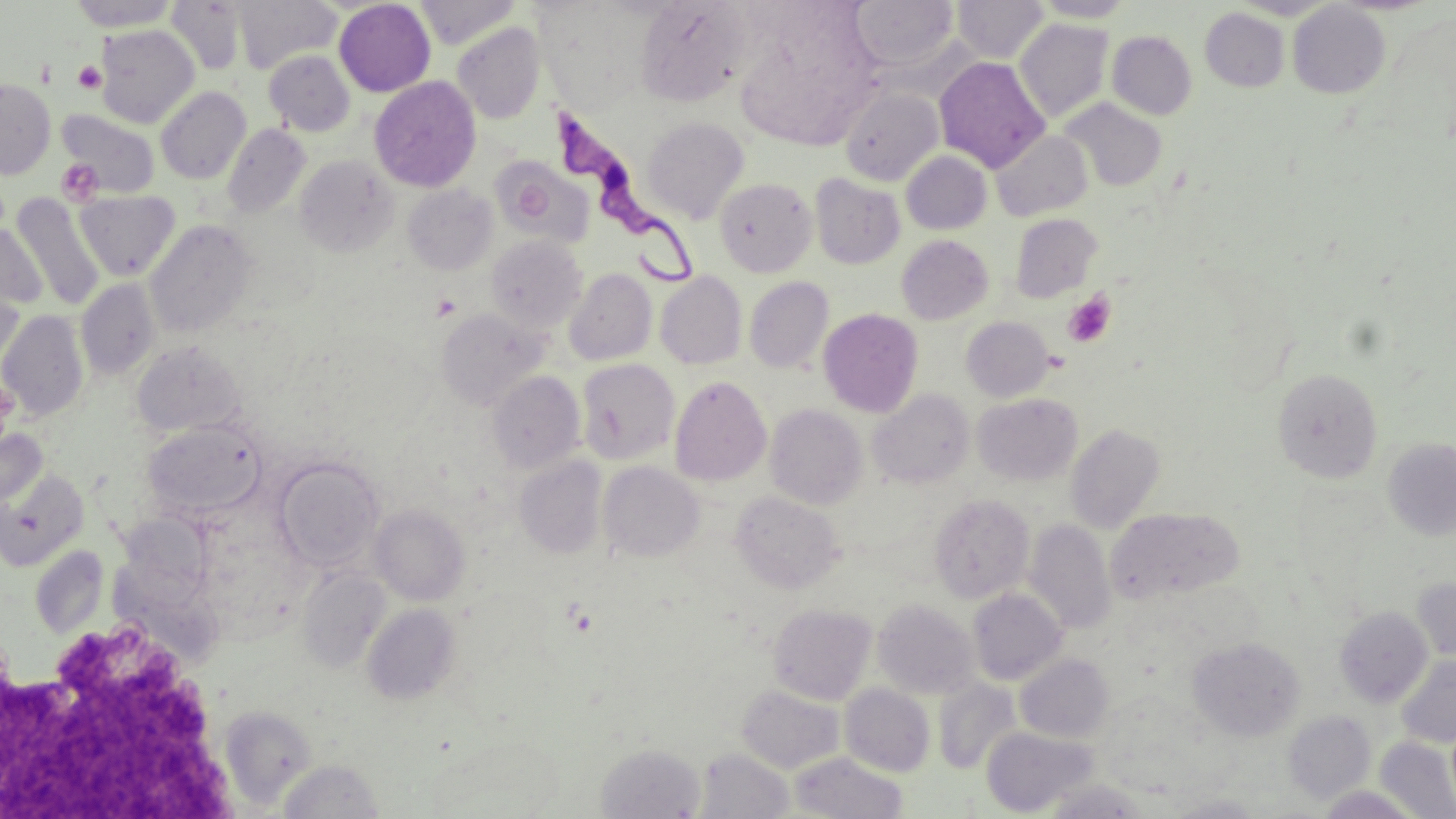
slide_level_diagnosis: Trypanosoma brucei
magnification: 1000x
preparation: thin blood smear
trypanosoma_brucei_locations: 'approximate bounding boxes as (x1,y1)-(x2,y2) corner pairs in pixels: (552,105)-(702,290)'
image_size: 1456×819 pixels
uninfected_red_blood_cell_locations: 'approximate bounding boxes as (x1,y1)-(x2,y2) corner pairs in pixels: (68,0)-(178,31), (233,0)-(341,74), (414,0)-(519,49), (635,0)-(750,106), (952,0)-(1049,63), (166,1)-(246,75), (334,1)-(436,97), (851,1)-(958,71), (1031,1)-(1137,22), (1288,2)-(1390,98), (1200,8)-(1290,92), (1013,18)-(1114,123), (451,22)-(545,124), (95,25)-(199,128), (1107,31)-(1197,119), (263,50)-(355,136), (935,56)-(1050,172), (369,76)-(481,192), (0,79)-(56,179), (156,86)-(251,184), (840,87)-(943,186), (1061,98)-(1167,191), (58,109)-(160,199), (642,116)-(749,223), (222,124)-(311,218), (991,130)-(1093,221), (902,151)-(991,234), (294,154)-(399,257), (491,157)-(594,247), (810,173)-(905,269), (715,177)-(817,277), (402,184)-(497,275), (74,191)-(180,281), (8,194)-(106,310), (1009,213)-(1103,302), (145,219)-(257,338), (0,224)-(47,314), (485,235)-(587,333), (896,235)-(993,325), (1,268)-(27,371), (564,268)-(656,366), (655,272)-(748,369), (744,276)-(834,373), (75,279)-(160,380), (436,308)-(549,410), (818,308)-(923,417), (0,311)-(88,421), (961,316)-(1054,402), (132,341)-(246,437), (576,359)-(680,465), (1273,368)-(1383,482), (486,370)-(585,474), (670,376)-(772,487), (868,389)-(974,489), (972,393)-(1082,486), (765,403)-(868,510), (143,419)-(266,519), (1066,423)-(1166,533), (0,427)-(47,512), (1383,438)-(1456,541), (273,456)-(384,571), (514,456)-(607,559), (598,461)-(704,562), (0,468)-(89,571), (731,490)-(845,593), (928,493)-(1036,603), (368,504)-(470,605), (1106,507)-(1244,605), (121,514)-(220,615), (1024,518)-(1116,634), (30,546)-(108,638), (297,566)-(391,673), (1411,578)-(1456,663), (967,588)-(1068,685), (872,599)-(979,699), (361,603)-(461,705), (768,603)-(877,705), (1334,605)-(1433,707), (1187,636)-(1306,741), (1015,653)-(1114,743), (1396,656)-(1456,748), (933,678)-(1021,775), (736,684)-(844,773), (839,684)-(935,776), (218,705)-(317,809), (1283,711)-(1376,804), (981,727)-(1098,816), (1375,736)-(1456,819), (596,743)-(706,818), (695,748)-(795,818), (788,751)-(909,818), (276,758)-(387,819), (1040,779)-(1151,818), (1316,785)-(1425,819), (1162,794)-(1268,818)'
stain: May-Grünwald-Giemsa
field_of_view: one of a larger specimen
platelet_locations: 'approximate bounding boxes as (x1,y1)-(x2,y2) corner pairs in pixels: (73,61)-(107,93), (55,158)-(103,206), (1063,291)-(1116,347), (0,621)-(229,818)'
modality: optical microscopy